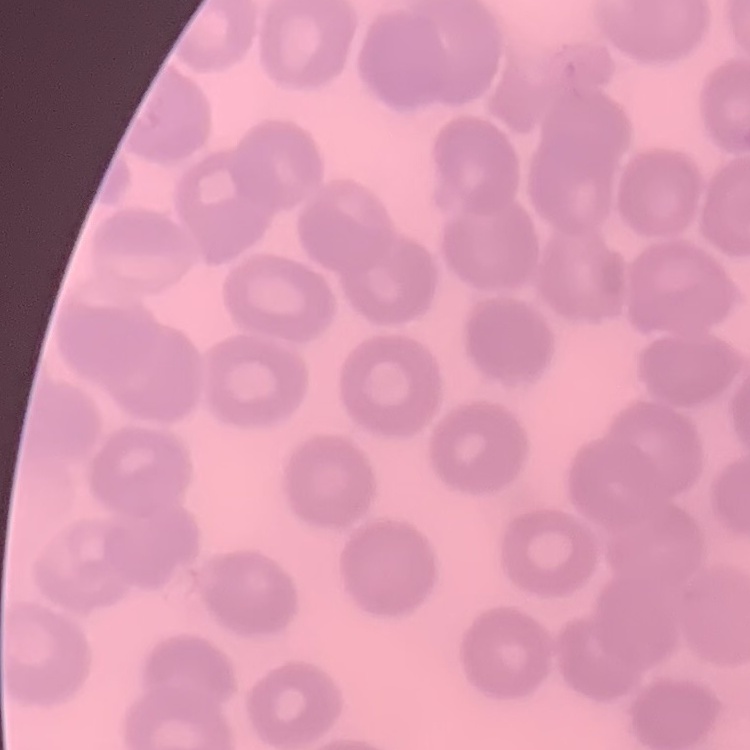

{
  "red_blood_cell_morphology": "no rouleaux formation",
  "image_type": "square crop of a larger photomicrograph",
  "preparation": "thin blood smear",
  "stain": "Field's or Giemsa"
}